Outline every leukocyte.
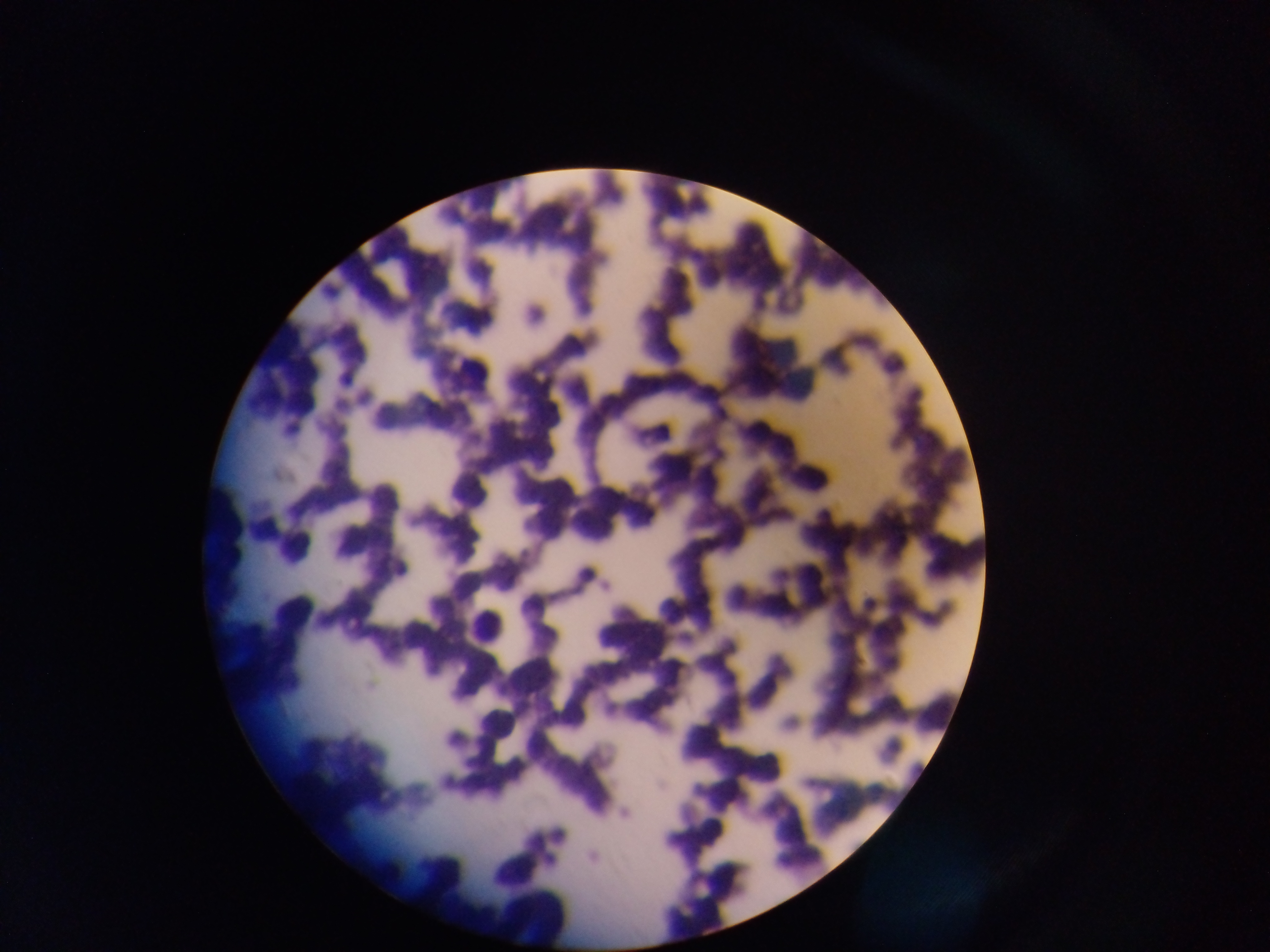

Approximate bounding boxes as (left, top, right, bottom) in pixels.
Leukocytes: (446, 350, 493, 391), (791, 452, 823, 496), (439, 453, 506, 509), (273, 533, 306, 560), (467, 557, 508, 652).

Image is 1270×952 pixels. Collected in Ghana. Thin blood film. Single field of view. Mobile-phone photograph taken through the microscope.